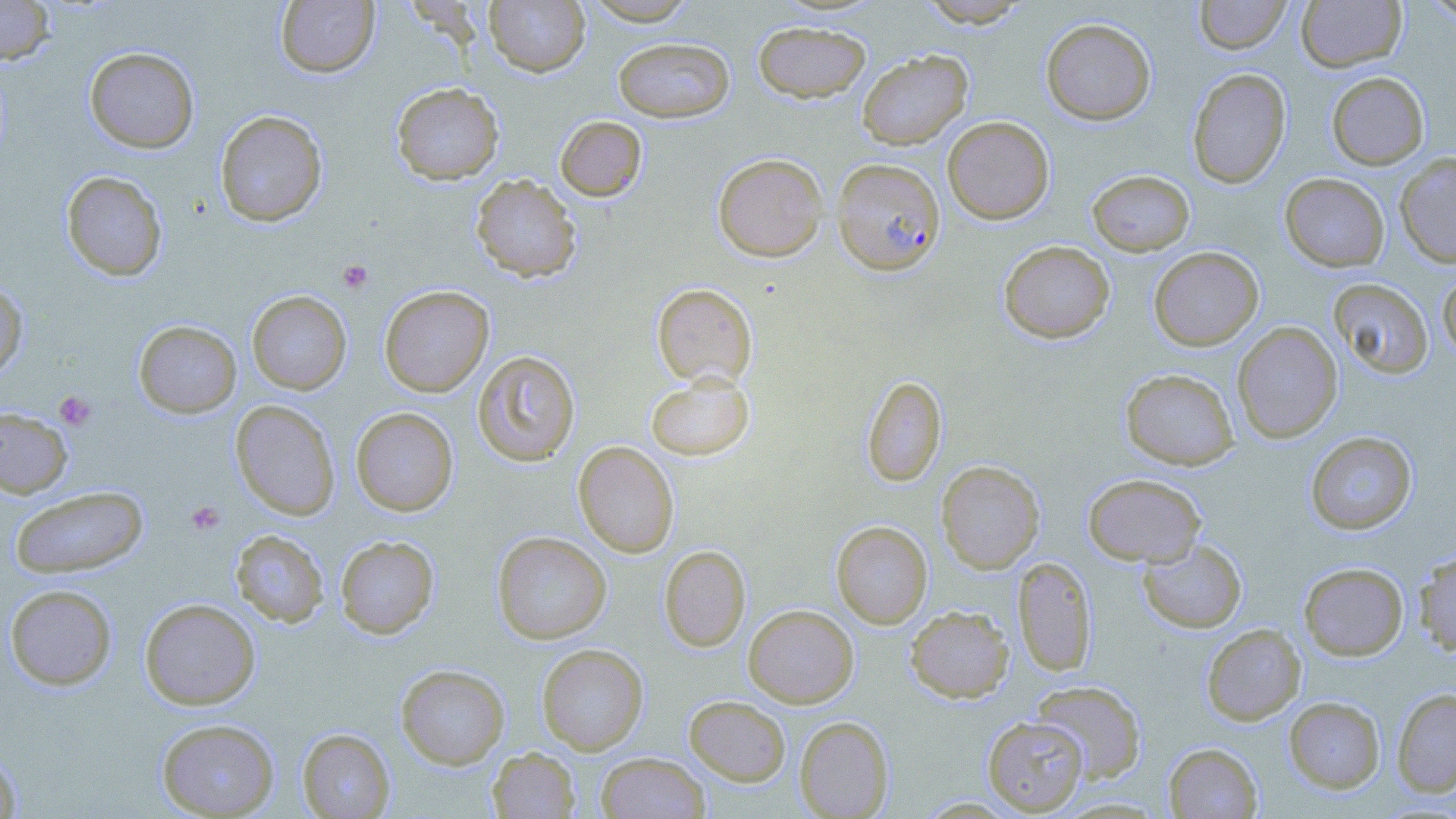
Summary:
  - Coordinate format: approximate bounding boxes as (x1, y1, x2, y2) in pixels
  - Platelet locations: (337, 260, 373, 293), (54, 390, 97, 431), (186, 501, 226, 536)
  - Plasmodium falciparum-infected red blood cell locations: (831, 157, 945, 276)
  - Uninfected red blood cell locations: (0, 0, 56, 64), (275, 0, 380, 78), (484, 0, 591, 77), (582, 0, 699, 25), (917, 0, 1032, 27), (1194, 0, 1290, 54), (1296, 0, 1407, 73), (1420, 0, 1456, 23), (1041, 18, 1156, 125), (753, 21, 871, 103), (613, 37, 734, 122), (84, 46, 199, 153), (857, 50, 972, 149), (1187, 67, 1291, 188), (1326, 72, 1429, 169), (391, 82, 504, 184), (214, 110, 328, 227), (555, 115, 648, 202), (942, 116, 1054, 224), (712, 152, 828, 261), (1395, 152, 1456, 267), (1087, 169, 1195, 256), (60, 170, 168, 281), (1279, 173, 1390, 272), (470, 174, 581, 283), (998, 240, 1114, 343), (1148, 246, 1264, 350), (1437, 267, 1456, 364), (1328, 278, 1433, 379), (0, 282, 28, 381), (651, 282, 758, 387), (379, 286, 494, 397), (247, 290, 351, 395), (133, 320, 241, 418), (1232, 322, 1343, 443), (472, 350, 581, 467), (1120, 368, 1239, 470), (645, 374, 755, 461), (862, 375, 947, 487), (230, 400, 341, 520), (0, 406, 73, 498), (350, 407, 458, 516), (1305, 431, 1417, 535), (573, 441, 679, 558), (936, 460, 1045, 573), (1083, 473, 1206, 566), (10, 486, 148, 579), (831, 521, 932, 628), (229, 529, 329, 628), (492, 531, 611, 644), (334, 535, 440, 639), (1137, 538, 1247, 633), (659, 545, 751, 652), (1414, 548, 1456, 656), (1012, 556, 1097, 676), (1298, 562, 1409, 660), (4, 584, 118, 690), (140, 598, 260, 710), (743, 604, 859, 707), (905, 605, 1014, 703), (1201, 623, 1306, 725), (536, 643, 648, 754), (396, 664, 510, 769), (1030, 680, 1147, 782), (1392, 688, 1456, 797), (684, 695, 790, 786), (1284, 696, 1385, 793), (794, 715, 893, 818), (982, 716, 1089, 815), (155, 718, 280, 818), (297, 728, 395, 818), (1164, 743, 1262, 818), (0, 747, 22, 818), (487, 747, 580, 818), (596, 752, 710, 819), (1051, 796, 1171, 818), (915, 797, 1020, 818)
  - Slide-level diagnosis: Plasmodium falciparum
  - Image size: 1456×819 pixels
  - Modality: light microscopy
  - Preparation: thin blood film
  - Stain: May-Grünwald-Giemsa
  - Field of view: one of a larger specimen
  - Magnification: 1000x